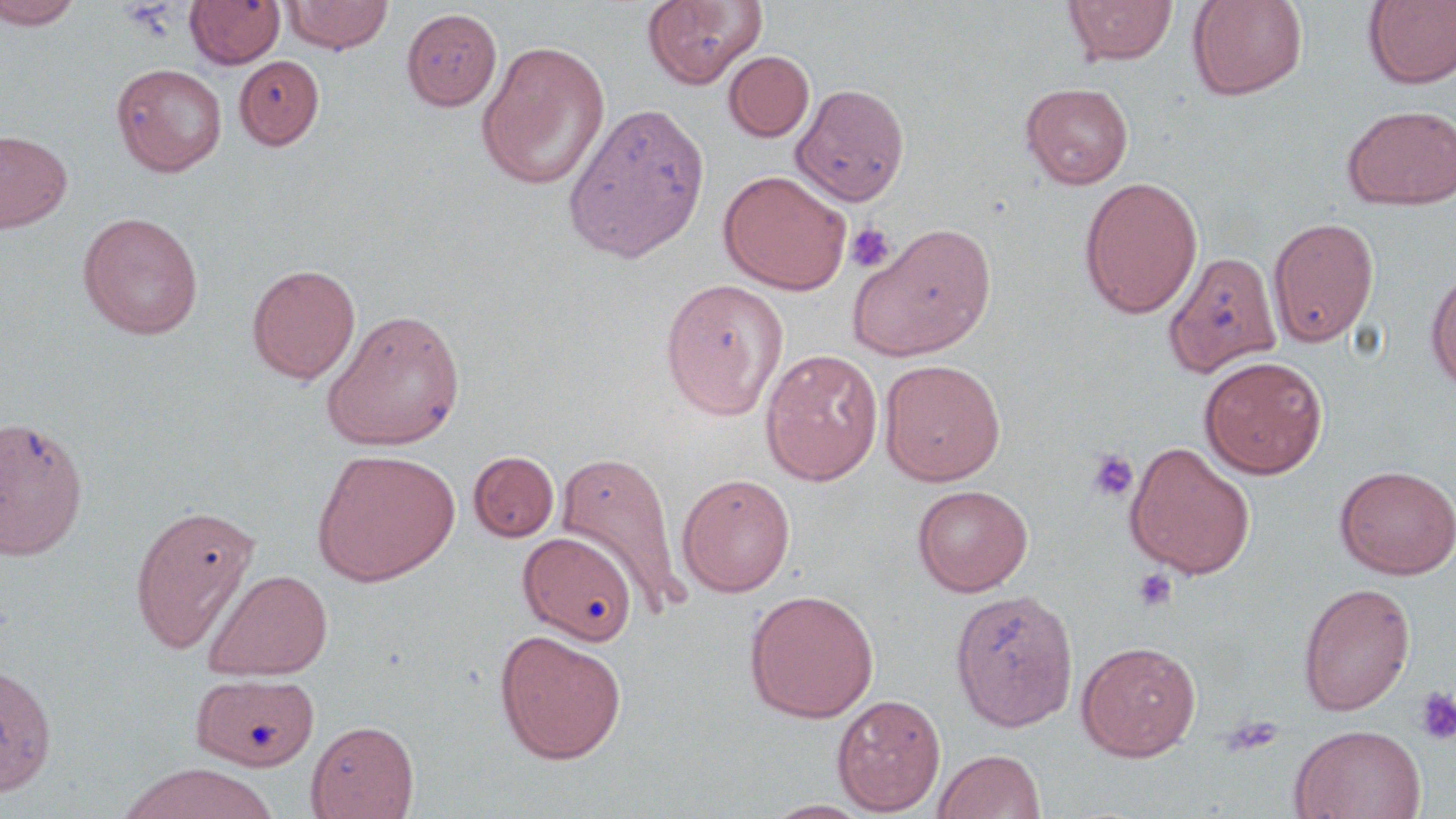 Approximate bounding boxes as [x1, y1, x2, y2] in pixels. Uninfected red blood cell locations: [0, 0, 82, 29], [283, 0, 394, 54], [642, 0, 768, 89], [1064, 0, 1177, 65], [1187, 0, 1309, 101], [1362, 0, 1456, 89], [185, 1, 286, 69], [401, 7, 503, 111], [476, 40, 611, 190], [724, 50, 815, 142], [235, 55, 324, 150], [111, 63, 226, 176], [791, 82, 910, 206], [1021, 82, 1134, 189], [562, 100, 711, 263], [1341, 103, 1456, 210], [0, 129, 72, 233], [718, 170, 851, 295], [1079, 176, 1203, 318], [77, 211, 203, 340], [1268, 215, 1380, 346], [847, 221, 997, 361], [1164, 250, 1283, 378], [246, 263, 361, 384], [1425, 266, 1456, 396], [660, 279, 789, 420], [322, 308, 466, 450], [760, 348, 884, 485], [1199, 355, 1328, 479], [879, 359, 1006, 486], [0, 414, 89, 560], [1125, 441, 1256, 579], [312, 448, 460, 586], [554, 448, 688, 616], [469, 451, 559, 542], [1334, 464, 1456, 579], [676, 473, 796, 597], [912, 484, 1033, 597], [130, 503, 260, 653], [519, 531, 638, 645], [204, 568, 333, 681], [1299, 582, 1416, 716], [744, 588, 879, 723], [950, 589, 1079, 732], [494, 629, 627, 765], [1076, 640, 1202, 761], [0, 660, 60, 803], [192, 673, 320, 771], [831, 694, 946, 814], [306, 719, 419, 819], [1290, 724, 1426, 819], [932, 748, 1046, 818], [119, 762, 276, 819], [758, 800, 879, 818]. Platelet locations: [846, 221, 897, 273], [1088, 450, 1138, 501], [1133, 568, 1178, 612], [1414, 687, 1456, 745], [1219, 715, 1285, 757]. Slide-level diagnosis: negative for blood parasites. May-Grünwald-Giemsa-stained preparation. 1000x magnification. Thin blood smear. Light microscopy. Single field of view. Image is 1456×819 pixels.